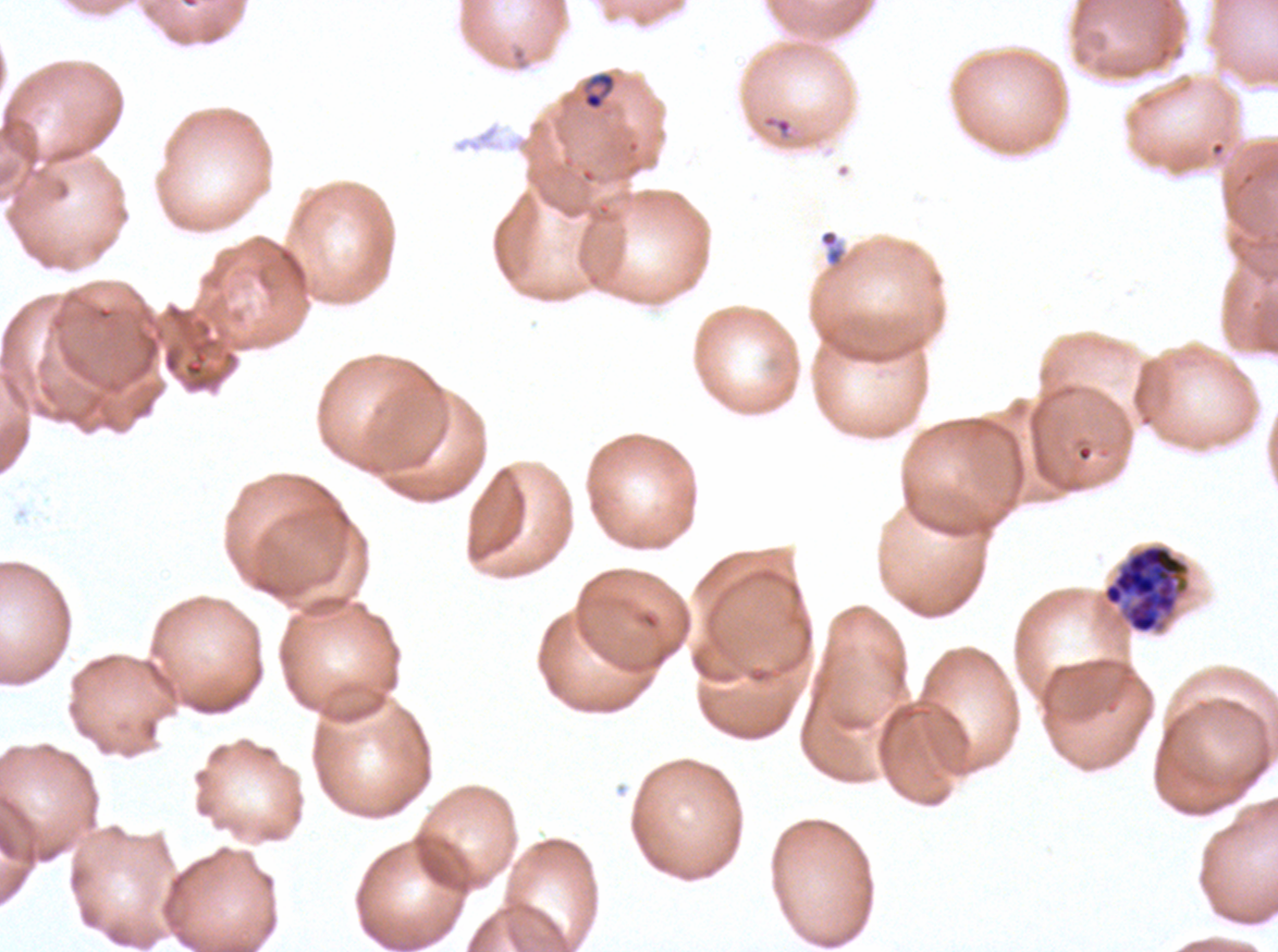

{
  "preparation": "thin blood smear",
  "late_schizont_locations": "approximate bounding rectangles given as corner coordinates in pixels from the top-left: (x1=1101, y1=543, x2=1190, y2=634)",
  "life_cycle_stages_observed": "ring, late schizont",
  "ring_locations": "approximate bounding rectangles given as corner coordinates in pixels from the top-left: (x1=582, y1=71, x2=616, y2=111)",
  "specimen": "P. falciparum from a patient in The Gambia, cultured ex vivo for 24 to 48 hours",
  "field_of_view": "sub-image separated from a larger composite",
  "stain": "Giemsa",
  "image_size": "1278×952 pixels",
  "debris_locations": "approximate bounding rectangles given as corner coordinates in pixels from the top-left: (x1=818, y1=228, x2=847, y2=268)"
}